Name the cell type shown.
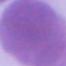

An erythrocyte.

magnification = 1000x
modality = photomicrograph